Name the blood parasite species.
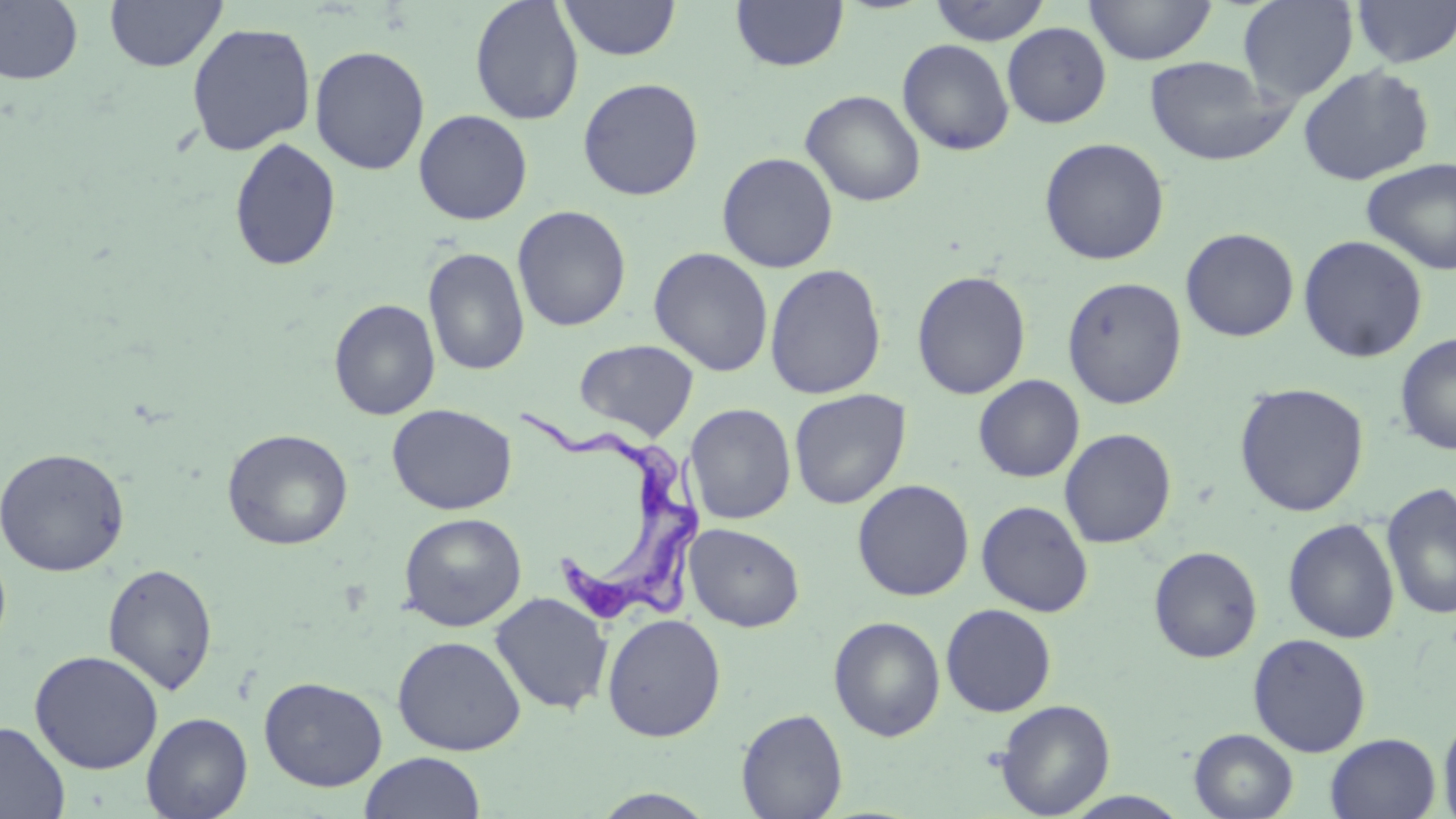
Trypanosoma brucei.

magnification = 1000x
field of view = one of a larger specimen
Trypanosoma brucei locations = approximate bounding boxes as named x1/y1/x2/y2 corners in pixels: (x1=519, y1=406, x2=707, y2=634)
preparation = thin blood film
modality = optical microscopy
stain = May-Grünwald-Giemsa
uninfected red blood cell locations = approximate bounding boxes as named x1/y1/x2/y2 corners in pixels: (x1=0, y1=0, x2=84, y2=86), (x1=104, y1=0, x2=227, y2=72), (x1=469, y1=0, x2=584, y2=125), (x1=557, y1=0, x2=681, y2=62), (x1=731, y1=0, x2=848, y2=72), (x1=928, y1=0, x2=1052, y2=45), (x1=1084, y1=0, x2=1217, y2=66), (x1=1237, y1=0, x2=1359, y2=102), (x1=1351, y1=0, x2=1456, y2=69), (x1=185, y1=21, x2=316, y2=156), (x1=1002, y1=22, x2=1112, y2=128), (x1=897, y1=39, x2=1014, y2=156), (x1=309, y1=45, x2=430, y2=176), (x1=1144, y1=56, x2=1291, y2=167), (x1=1297, y1=64, x2=1435, y2=186), (x1=577, y1=77, x2=704, y2=200), (x1=800, y1=90, x2=926, y2=207), (x1=413, y1=109, x2=533, y2=225), (x1=1038, y1=136, x2=1170, y2=266), (x1=229, y1=137, x2=342, y2=272), (x1=716, y1=152, x2=838, y2=273), (x1=1360, y1=157, x2=1456, y2=275), (x1=512, y1=205, x2=632, y2=332), (x1=1180, y1=227, x2=1300, y2=342), (x1=1298, y1=234, x2=1428, y2=363), (x1=423, y1=247, x2=530, y2=377), (x1=649, y1=247, x2=774, y2=377), (x1=764, y1=263, x2=887, y2=400), (x1=912, y1=270, x2=1031, y2=399), (x1=1062, y1=276, x2=1187, y2=409), (x1=329, y1=298, x2=441, y2=421), (x1=1394, y1=333, x2=1456, y2=454), (x1=574, y1=339, x2=699, y2=440), (x1=973, y1=374, x2=1085, y2=483), (x1=1234, y1=382, x2=1370, y2=517), (x1=789, y1=388, x2=911, y2=509), (x1=387, y1=403, x2=517, y2=515), (x1=684, y1=403, x2=797, y2=525), (x1=1059, y1=427, x2=1177, y2=548), (x1=222, y1=428, x2=353, y2=550), (x1=0, y1=446, x2=129, y2=576), (x1=852, y1=479, x2=975, y2=601), (x1=1381, y1=482, x2=1456, y2=620), (x1=976, y1=500, x2=1094, y2=617), (x1=398, y1=512, x2=526, y2=632), (x1=1282, y1=518, x2=1400, y2=644), (x1=684, y1=523, x2=805, y2=632), (x1=1148, y1=545, x2=1263, y2=663), (x1=103, y1=563, x2=217, y2=696), (x1=490, y1=592, x2=613, y2=715), (x1=940, y1=603, x2=1057, y2=717), (x1=602, y1=613, x2=726, y2=742), (x1=828, y1=616, x2=946, y2=741), (x1=1247, y1=632, x2=1372, y2=757), (x1=392, y1=635, x2=526, y2=755), (x1=29, y1=650, x2=164, y2=775), (x1=258, y1=676, x2=388, y2=792), (x1=994, y1=699, x2=1115, y2=817), (x1=736, y1=708, x2=848, y2=819), (x1=141, y1=712, x2=253, y2=819), (x1=1438, y1=712, x2=1456, y2=819), (x1=0, y1=721, x2=69, y2=819), (x1=1189, y1=729, x2=1298, y2=818), (x1=1325, y1=733, x2=1441, y2=819), (x1=359, y1=751, x2=486, y2=819), (x1=589, y1=788, x2=720, y2=818), (x1=1062, y1=791, x2=1192, y2=819)
image size = 1456×819 pixels